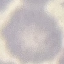

{
  "result": "no malaria parasites detected",
  "capture": "smartphone camera at the microscope eyepiece",
  "stain": "Giemsa",
  "preparation": "thin blood smear",
  "image_type": "cell patch, automatically extracted from a larger field of view and resized to 64 × 64 pixels"
}